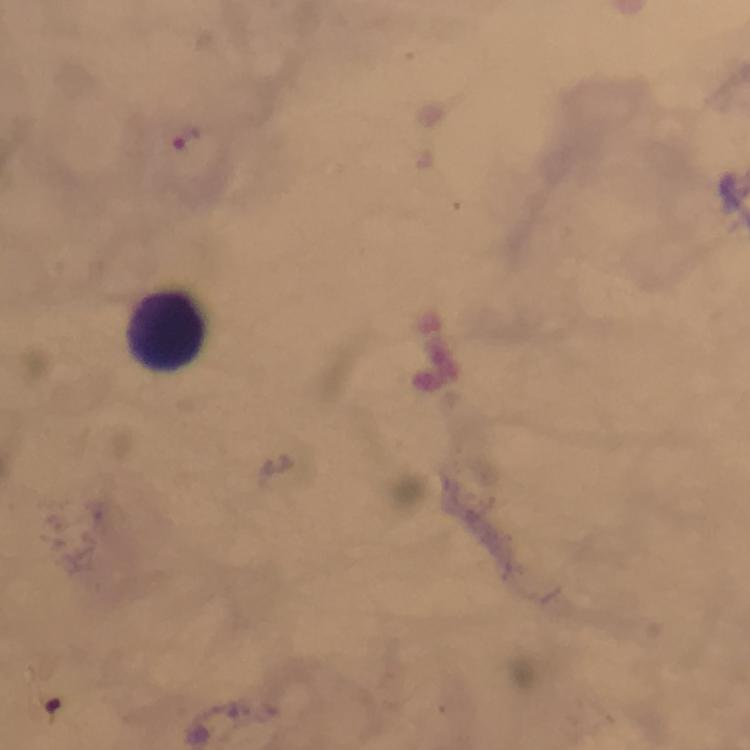

context: from a malaria diagnostic workup
immersion_oil: applied
capture: smartphone mounted on the microscope
stain: Giemsa
preparation: thick blood film
leukocyte_locations: 'approximate centers as (x, y) in pixels: (165, 331)'
cropped_from: one field of view
image_size: 750×750 pixels
magnification: 100x
plasmodium_parasites: none detected